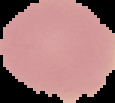
image type = segmented cell region with the area outside set to black
malaria status = uninfected
image size = 115×103 pixels
preparation = thin blood film